Give the position of every Plasmodium parasite visible.
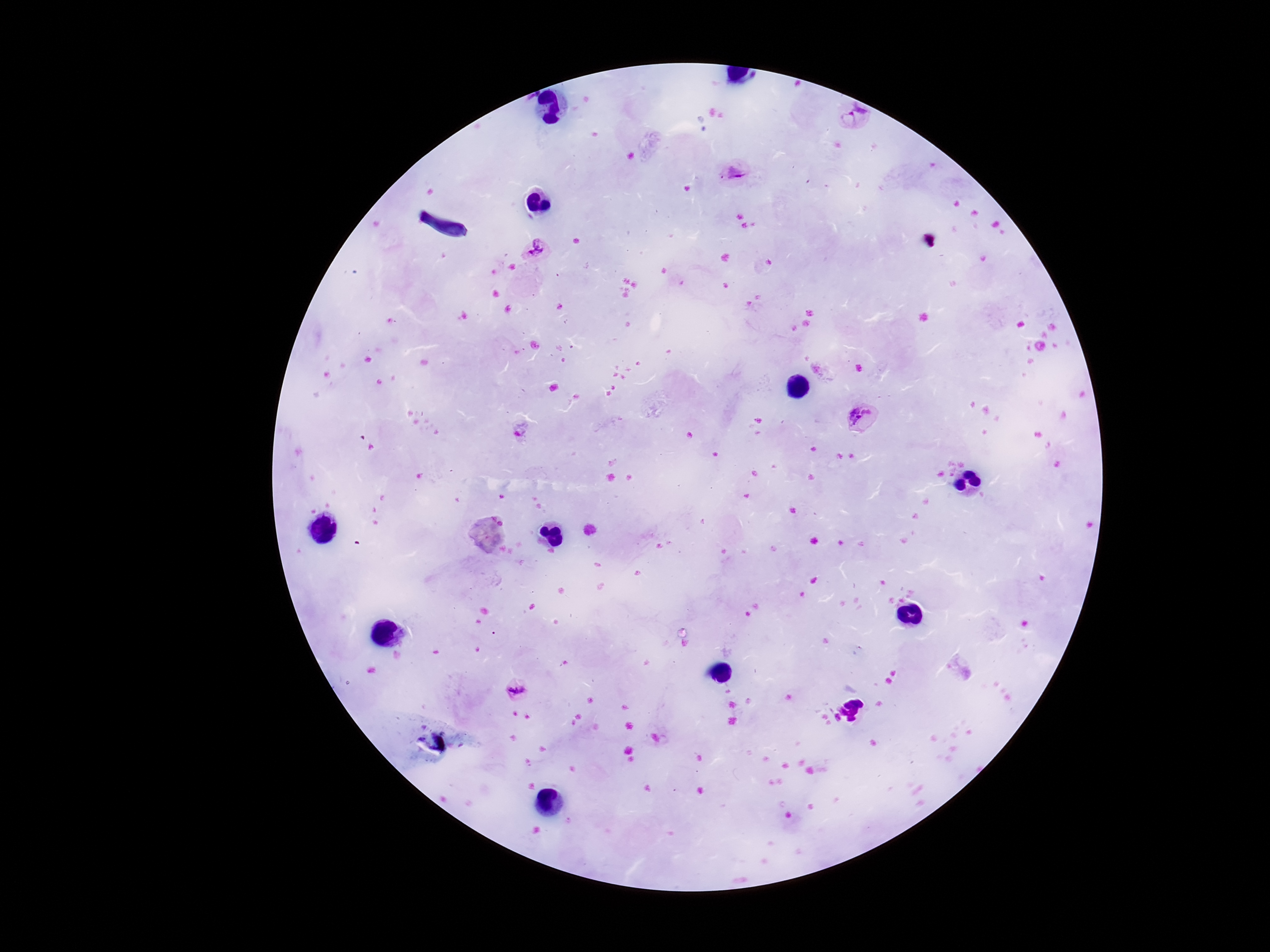

Approximate object centers, in pixels from the top-left corner.
Plasmodium parasites: (x=852, y=118), (x=737, y=173), (x=532, y=248), (x=860, y=418), (x=520, y=429), (x=517, y=691).

preparation = thick peripheral-blood smear
field of view = single
capture = smartphone camera through the microscope eyepiece
magnification = 100x
stain = Giemsa
image size = 1270×952 pixels
patient malaria status = infected